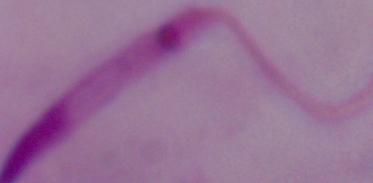
Captured at 1000x magnification. A Leishmania parasite is shown. Micrograph.